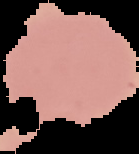

Cell region segmented out of the field of view; the surrounding area is masked to black. Result: negative for malaria parasites. Image is 139×154 pixels. From a thin blood film.